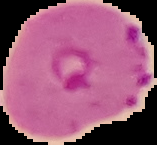

Summary:
  - Preparation: thin blood film
  - Image size: 157×145 pixels
  - Image type: cell region segmented out of the field of view; surrounding area masked to black
  - Result: Plasmodium parasites detected